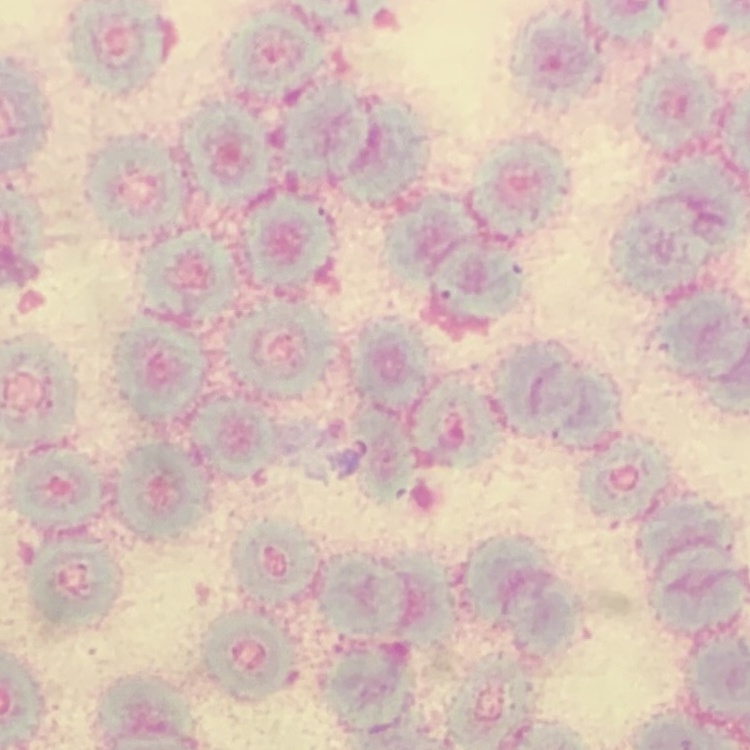
{
  "red_blood_cell_morphology": "rouleaux formation",
  "preparation": "thin blood smear",
  "image_type": "square crop of a larger photomicrograph",
  "stain": "Field's or Giemsa"
}